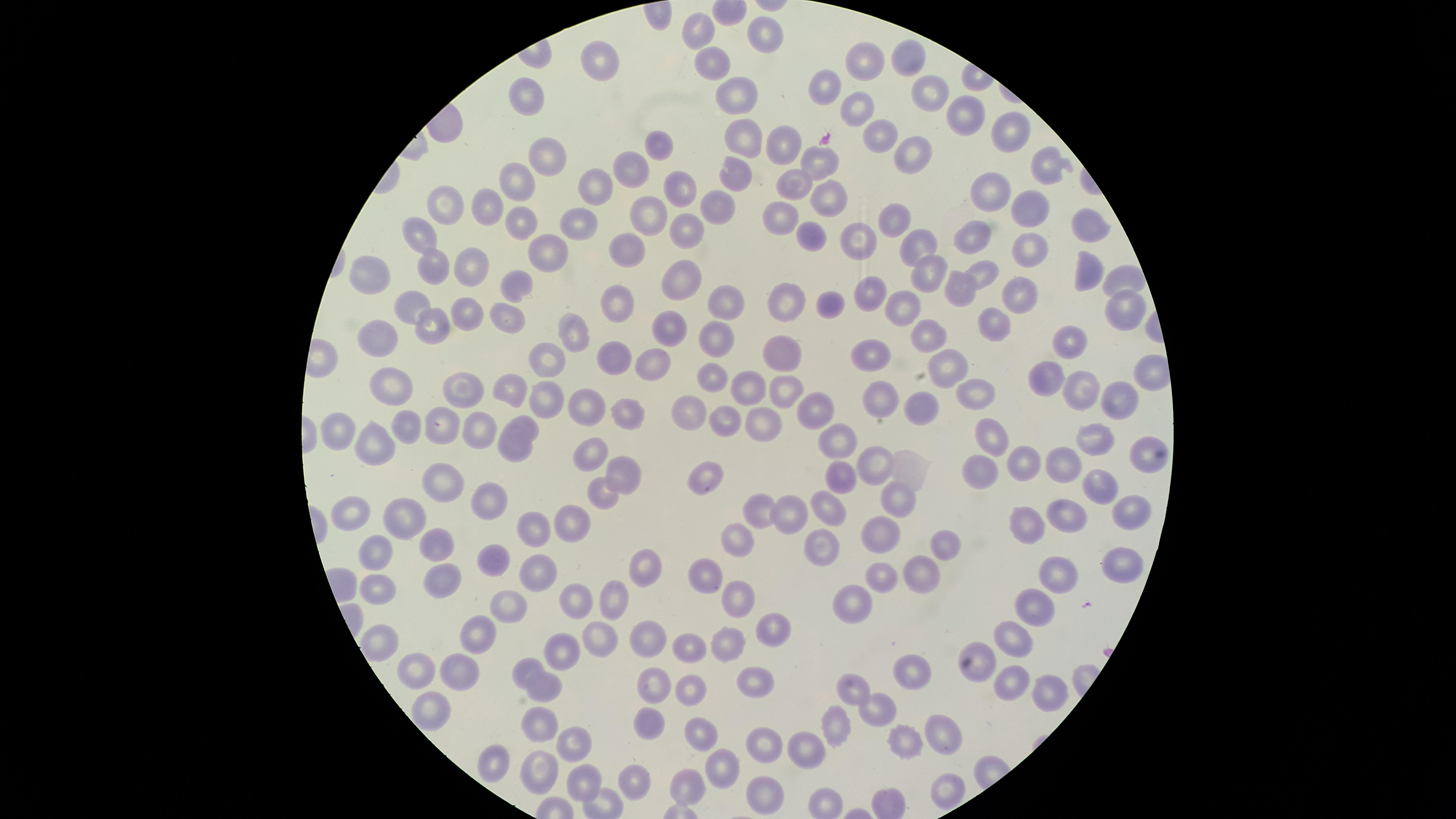
presence = no malaria parasites detected
visible region = circular
stain = Giemsa
capture = smartphone photograph through the microscope eyepiece
field of view = single
image size = 1456×819 pixels
preparation = thin blood smear
uninfected RBCs = approximate marker points as {x, y} in pixels: {703, 29}, {769, 32}, {911, 57}, {602, 61}, {712, 61}, {864, 61}, {826, 81}, {732, 86}, {935, 87}, {528, 95}, {855, 99}, {963, 112}, {1010, 129}, {741, 138}, {881, 138}, {788, 139}, {653, 144}, {909, 149}, {550, 159}, {819, 160}, {1052, 164}, {626, 174}, {733, 174}, {517, 180}, {793, 184}, {599, 185}, {684, 190}, {996, 192}, {826, 197}, {719, 202}, {486, 204}, {449, 206}, {1027, 206}, {643, 212}, {894, 215}, {783, 217}, {518, 222}, {568, 224}, {1089, 227}, {420, 230}, {691, 232}, {971, 234}, {810, 235}, {853, 243}, {924, 244}, {547, 248}, {626, 248}, {1028, 248}, {434, 266}, {684, 269}, {929, 269}, {467, 270}, {981, 270}, {1083, 270}, {369, 276}, {1121, 276}, {513, 284}, {960, 288}, {1021, 295}, {864, 297}, {728, 300}, {410, 304}, {613, 304}, {828, 304}, {910, 304}, {788, 305}, {1118, 306}, {462, 316}, {505, 316}, {996, 322}, {669, 324}, {577, 327}, {427, 328}, {937, 332}, {712, 333}, {1069, 338}, {377, 341}, {782, 349}, {876, 354}, {612, 357}, {549, 360}, {952, 362}, {654, 364}, {709, 374}, {1040, 375}, {1080, 385}, {783, 386}, {747, 387}, {393, 388}, {973, 388}, {508, 391}, {462, 392}, {543, 393}, {1117, 396}, {582, 401}, {883, 401}, {804, 405}, {626, 408}, {918, 408}, {686, 409}, {726, 415}, {526, 422}, {765, 422}, {408, 426}, {442, 426}, {478, 428}, {337, 430}, {993, 435}, {371, 443}, {1092, 444}, {835, 447}, {514, 451}, {589, 453}, {1148, 456}, {1020, 463}, {1061, 463}, {977, 464}, {874, 465}, {906, 467}, {702, 475}, {839, 476}, {454, 483}, {628, 483}, {1098, 485}, {598, 496}, {489, 500}, {896, 500}, {829, 510}, {355, 512}, {762, 514}, {1126, 515}, {793, 517}, {405, 519}, {565, 520}, {1027, 522}, {1068, 522}, {533, 526}, {877, 532}, {438, 542}, {941, 542}, {377, 543}, {739, 543}, {819, 549}, {499, 555}, {638, 563}, {535, 565}, {1118, 566}, {1061, 576}, {705, 578}, {883, 579}, {919, 580}, {436, 581}, {377, 592}, {736, 597}, {611, 600}, {857, 602}, {1035, 603}, {508, 604}, {576, 608}, {767, 627}, {479, 630}, {653, 637}, {599, 639}, {725, 641}, {1010, 642}, {378, 644}, {563, 649}, {691, 649}, {907, 665}, {977, 665}, {525, 667}, {414, 669}, {459, 671}, {654, 678}, {1001, 679}, {751, 682}, {542, 684}, {853, 687}, {693, 690}, {1040, 694}, {879, 709}, {425, 714}, {541, 725}, {836, 727}, {651, 728}, {942, 733}, {701, 735}, {908, 739}, {765, 740}, {808, 748}, {571, 750}, {486, 761}, {718, 768}, {539, 772}, {582, 781}, {638, 781}, {941, 785}, {685, 786}, {763, 789}